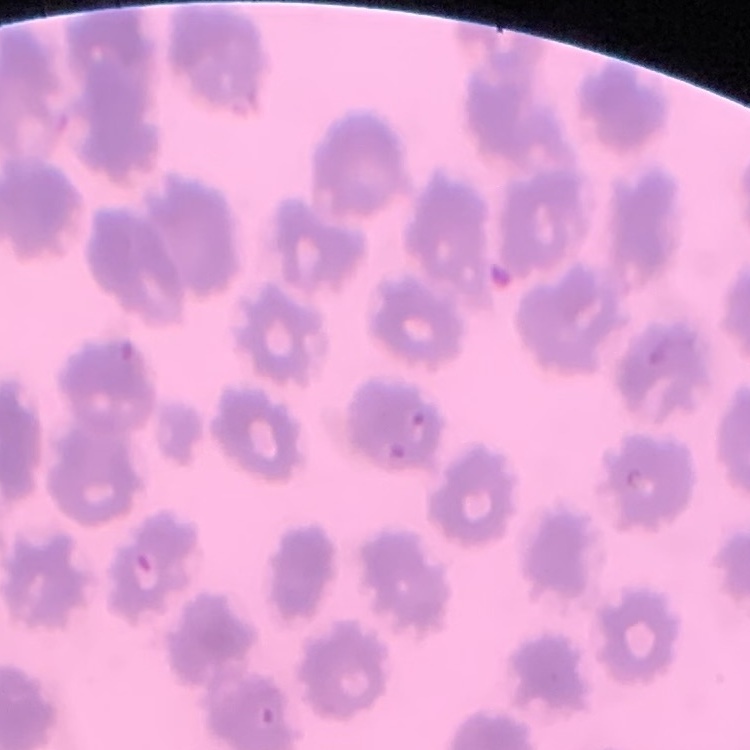

erythrocyte morphology = no rouleaux formation
preparation = thin peripheral smear
image type = one tile cut from a larger photomicrograph
stain = Field's or Giemsa